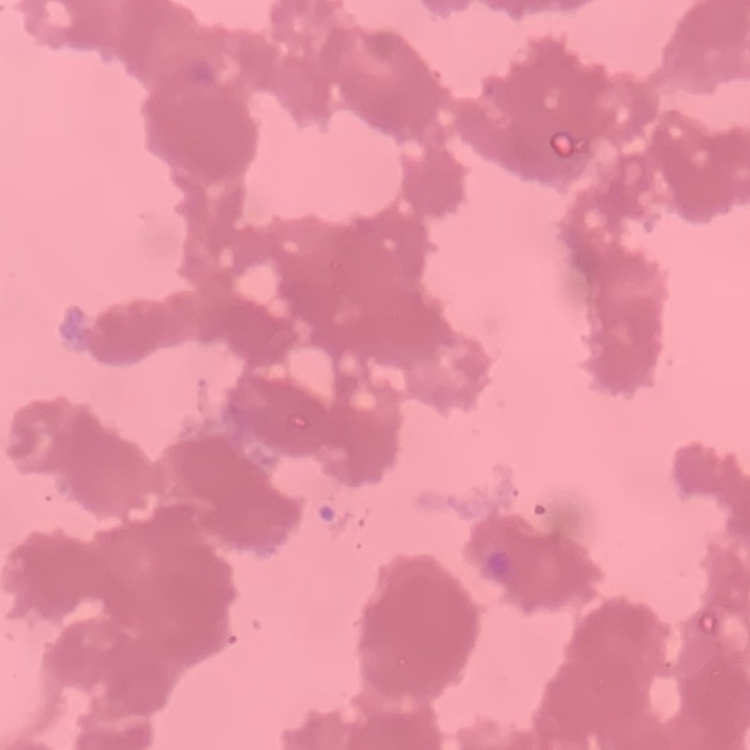

The erythrocytes exhibit rouleaux formation. One tile cut from a larger photomicrograph. Field's or Giemsa stain. Thin blood film.